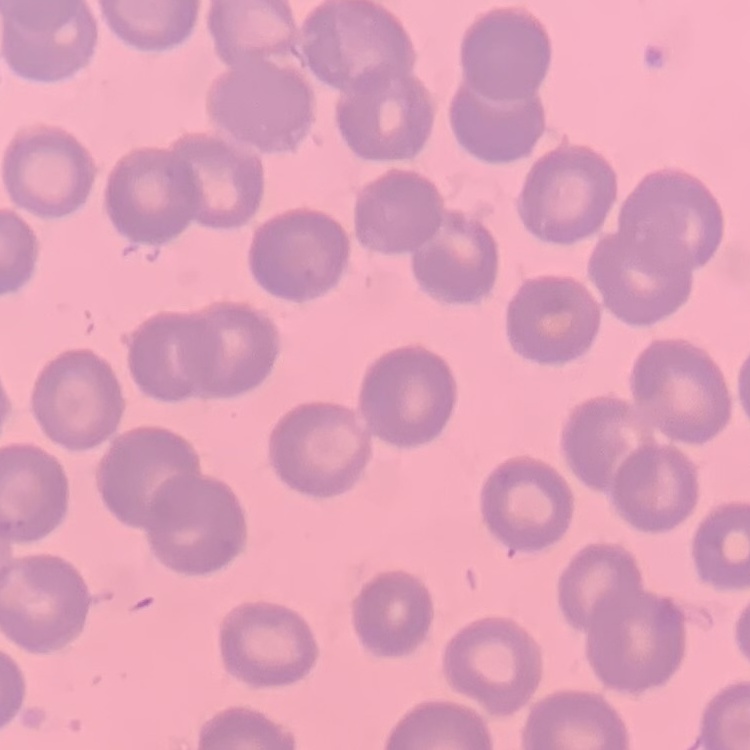

Summary:
  - Red blood cell morphology: no rouleaux formation
  - Stain: Field's or Giemsa
  - Image type: square crop of a larger photomicrograph
  - Preparation: thin blood smear